Point out each leukocyte.
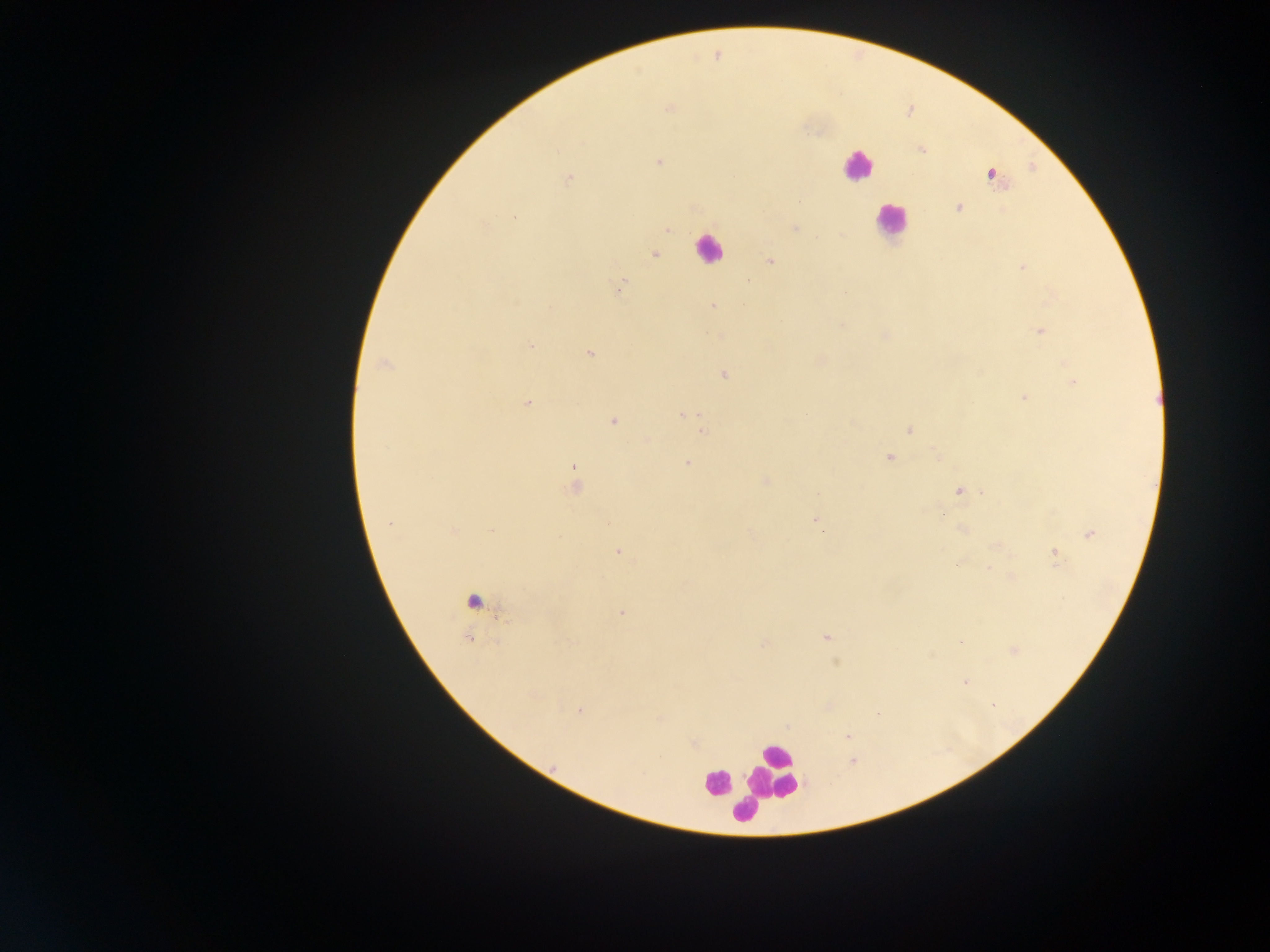
Approximate centers as {x, y} in pixels.
Leukocytes: {856, 166}, {891, 221}, {701, 254}, {782, 757}, {715, 781}, {768, 798}.

Malaria parasite locations: {804, 126}, {921, 150}, {659, 163}, {990, 174}, {568, 179}, {958, 208}, {514, 217}, {795, 227}, {668, 229}, {817, 235}, {655, 254}, {769, 261}, {1022, 266}, {749, 282}, {622, 283}, {846, 291}, {711, 305}, {842, 324}, {1039, 329}, {532, 343}, {591, 353}, {819, 359}, {382, 362}, {724, 374}, {1073, 382}, {1024, 397}, {528, 403}, {680, 416}, {612, 421}, {703, 430}, {908, 430}, {935, 454}, {889, 456}, {687, 464}, {574, 465}, {574, 474}, {766, 480}, {573, 485}, {957, 490}, {817, 493}, {939, 513}, {815, 519}, {389, 523}, {607, 523}, {961, 528}, {492, 531}, {454, 532}, {1089, 534}, {752, 535}, {998, 546}, {616, 550}, {1054, 553}, {990, 568}, {478, 600}, {622, 613}, {825, 637}, {762, 645}, {835, 662}, {964, 680}, {580, 709}, {660, 719}, {847, 736}, {694, 743}, {852, 760}. Image is 1270×952 pixels. Photographed through a microscope with a mobile-phone camera. Single field of view. Thick blood smear. Sample from Ghana.